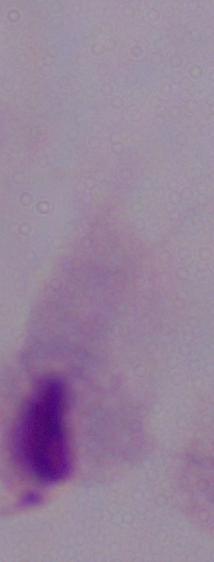

Summary:
  - Modality: photomicrograph
  - Identification: trichomonad
  - Magnification: 1000x